Identify the parasite.
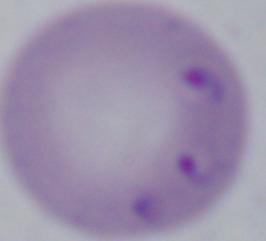

This is Babesia.

1000x magnification. Micrograph.